State the blood parasite species.
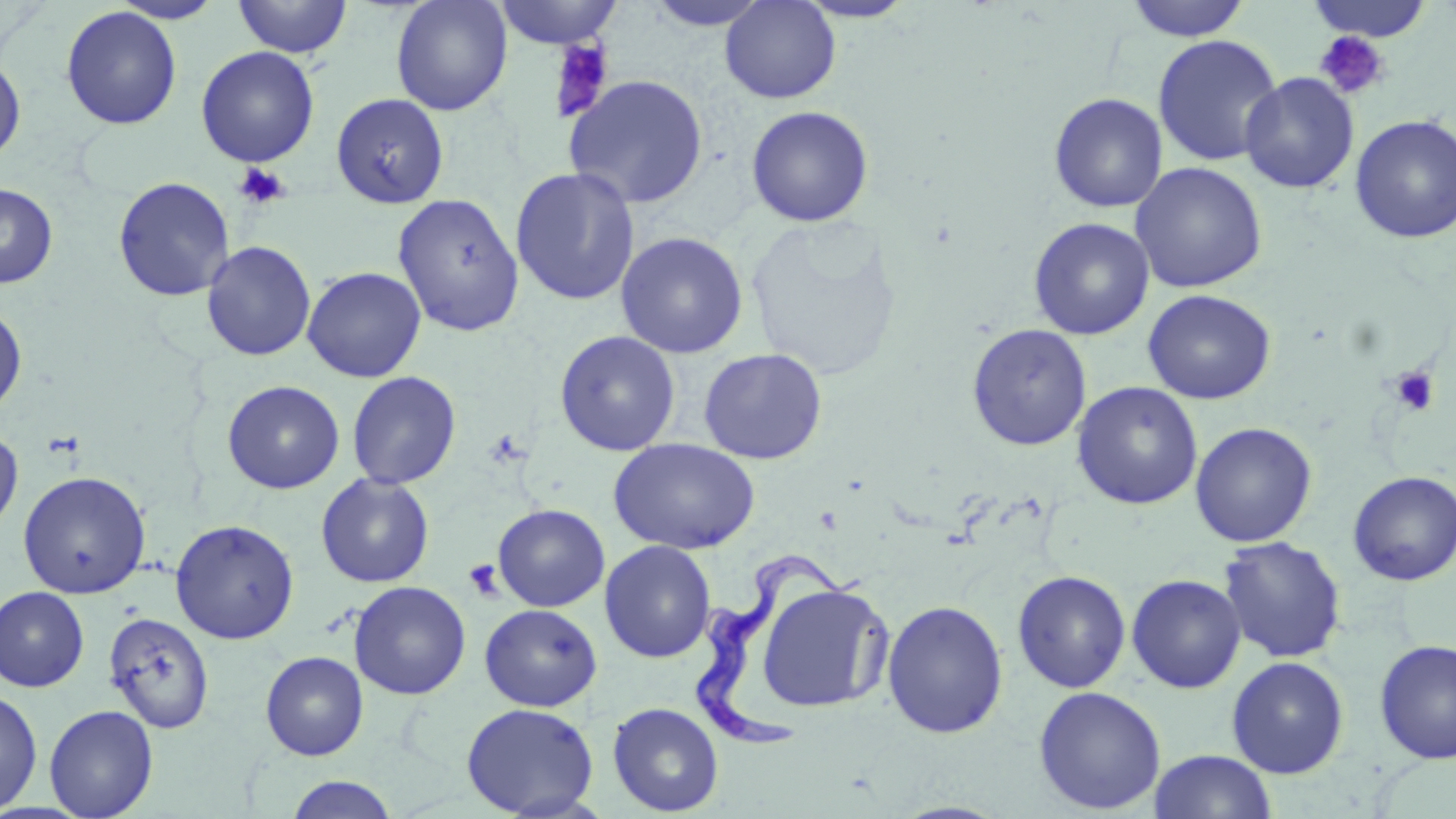
Trypanosoma brucei.

Summary:
  - Coordinate format: approximate bounding boxes as (x1,y1)-(x2,y2) corner pairs in pixels
  - Platelet locations: (1314,31)-(1391,101), (548,39)-(614,121), (233,162)-(290,209), (1389,366)-(1440,416), (463,559)-(504,602)
  - Uninfected red blood cell locations: (110,0)-(226,23), (232,0)-(352,58), (719,0)-(841,104), (1124,0)-(1251,41), (1305,0)-(1435,43), (391,1)-(512,116), (491,1)-(624,49), (642,1)-(775,32), (792,1)-(921,23), (61,6)-(182,130), (1152,35)-(1283,167), (195,46)-(320,167), (0,55)-(26,163), (1240,72)-(1359,194), (563,74)-(709,209), (331,92)-(449,208), (1048,92)-(1168,213), (745,105)-(874,228), (1349,113)-(1456,244), (1130,162)-(1267,293), (510,167)-(641,306), (113,176)-(235,301), (0,182)-(58,289), (392,193)-(524,337), (1028,217)-(1155,340), (744,218)-(903,383), (615,231)-(748,358), (201,241)-(316,361), (302,266)-(426,382), (1143,289)-(1276,404), (0,302)-(27,418), (966,323)-(1092,451), (554,330)-(680,455), (698,347)-(828,465), (347,371)-(461,490), (222,380)-(345,494), (1072,381)-(1203,510), (1190,422)-(1317,547), (0,426)-(23,536), (609,438)-(760,555), (1346,470)-(1455,586), (18,471)-(151,599), (316,473)-(434,588), (493,504)-(609,612), (170,519)-(300,644), (1218,537)-(1346,663), (600,540)-(716,662), (1012,570)-(1131,693), (1126,574)-(1247,694), (349,581)-(471,700), (755,582)-(894,715), (0,587)-(89,692), (882,599)-(1009,739), (479,604)-(602,711), (103,612)-(215,733), (1374,638)-(1456,764), (260,651)-(369,760), (1226,656)-(1348,778), (1033,686)-(1166,814), (0,688)-(42,814), (461,702)-(599,817), (607,702)-(724,816), (44,705)-(159,818), (1148,749)-(1277,819), (285,775)-(399,819)
  - Trypanosoma brucei locations: (692,552)-(871,757)
  - Image size: 1456×819 pixels
  - Field of view: single
  - Preparation: thin blood film
  - Stain: May-Grünwald-Giemsa
  - Magnification: 1000x
  - Modality: light microscopy